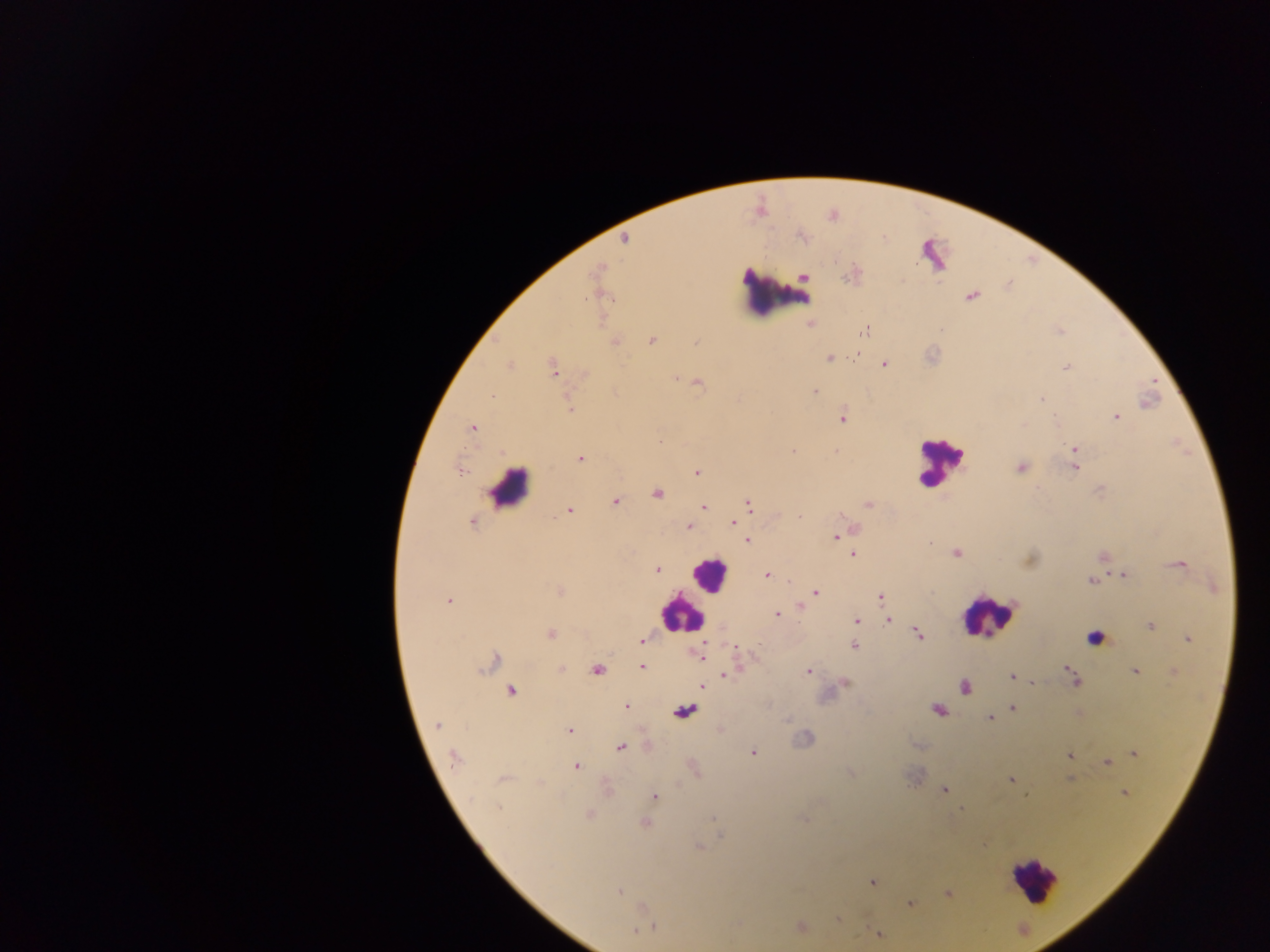
preparation = thick blood film
country = Ghana
field of view = single
image size = 1270×952 pixels
capture = mobile-phone photograph through a microscope
leukocyte locations = approximate centers as [x, y] in pixels: [773, 299], [942, 461], [510, 487], [713, 571], [988, 610], [679, 612], [1035, 886]
Plasmodium parasite locations = approximate centers as [x, y] in pixels: [801, 238], [623, 240], [804, 276], [844, 277], [584, 298], [866, 328], [1059, 329], [653, 340], [694, 341], [615, 342], [830, 357], [855, 357], [884, 363], [510, 364], [553, 368], [1067, 368], [675, 377], [699, 384], [1152, 384], [815, 390], [494, 395], [1040, 400], [569, 407], [844, 418], [1117, 418], [1056, 420], [472, 429], [1074, 448], [794, 450], [580, 457], [1020, 467], [1075, 468], [460, 469], [694, 471], [1099, 491], [658, 492], [614, 502], [867, 503], [703, 506], [750, 506], [568, 512], [799, 516], [473, 521], [735, 521], [688, 527], [835, 535], [748, 540], [931, 543], [956, 552], [852, 553], [1102, 557], [1179, 565], [657, 569], [1121, 574], [767, 575], [1090, 581], [815, 592], [812, 595], [879, 597], [449, 598], [799, 607], [777, 615], [888, 620], [856, 621], [1149, 626], [550, 633], [917, 634], [1187, 638], [642, 641], [854, 646], [735, 649], [701, 658], [495, 661], [642, 667], [560, 668], [481, 670], [596, 671], [1068, 671], [807, 672], [1134, 672], [724, 676], [1010, 676], [1073, 680], [846, 682], [1031, 683], [701, 686], [964, 687], [512, 691], [626, 706], [1012, 708], [937, 710], [788, 718], [989, 719], [436, 724], [569, 733], [622, 749], [753, 753], [1133, 753], [451, 757], [1069, 757], [1107, 762], [577, 767], [850, 773], [1069, 777], [502, 779], [1010, 780], [944, 789], [1123, 791], [655, 796], [1026, 797], [498, 808], [712, 818], [803, 819], [646, 823], [718, 838], [700, 848], [870, 882], [619, 893], [948, 894], [910, 903], [835, 920], [656, 926], [799, 927], [632, 932], [878, 934]